Give the extent of all Plasmodium ovale-infected red blood cells.
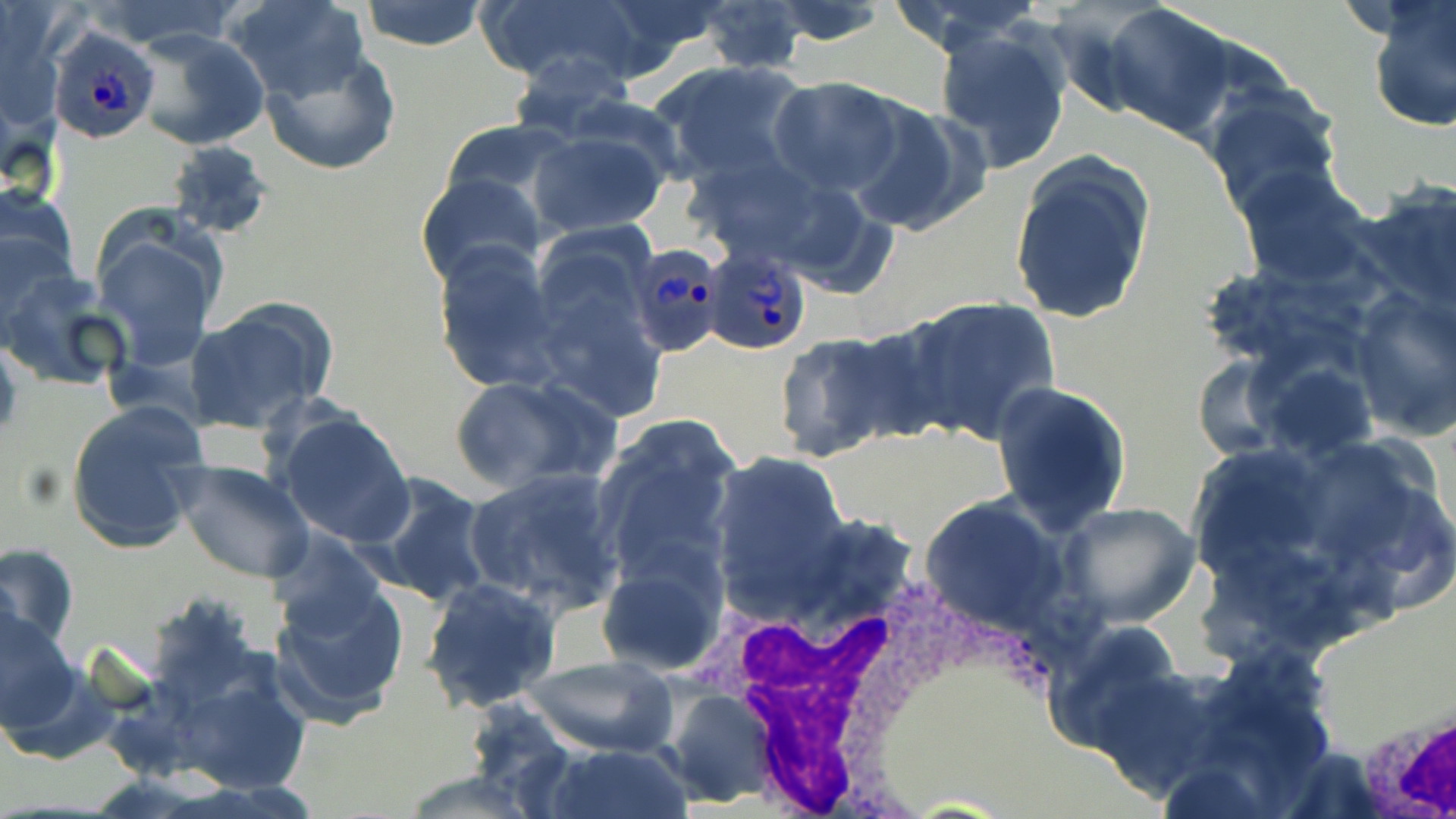
Approximate bounding boxes as [x1, y1, x2, y2] in pixels.
Plasmodium ovale-infected red blood cells: [47, 25, 163, 145], [633, 240, 723, 363], [701, 246, 815, 357].

slide-level diagnosis = Plasmodium ovale
stain = May-Grünwald-Giemsa
modality = optical microscopy
magnification = 1000x
uninfected red blood cell locations = approximate bounding boxes as [x1, y1, x2, y2] in pixels: [228, 0, 373, 105], [358, 0, 489, 52], [475, 0, 653, 91], [883, 0, 1050, 53], [1365, 0, 1455, 132], [693, 1, 811, 75], [764, 2, 893, 47], [1102, 3, 1236, 141], [933, 25, 1072, 174], [131, 29, 270, 152], [261, 51, 400, 177], [505, 52, 637, 140], [651, 59, 813, 188], [768, 76, 909, 198], [1199, 85, 1345, 216], [847, 99, 987, 238], [438, 119, 583, 217], [528, 125, 673, 237], [165, 139, 273, 241], [1009, 155, 1155, 324], [1234, 165, 1373, 289], [416, 174, 548, 292], [1356, 179, 1456, 309], [0, 185, 83, 319], [92, 220, 225, 372], [431, 241, 563, 393], [2, 273, 133, 393], [1347, 288, 1456, 441], [897, 297, 1061, 445], [181, 299, 336, 436], [769, 332, 913, 464], [0, 337, 21, 447], [1188, 350, 1296, 460], [1252, 359, 1381, 464], [447, 373, 614, 494], [991, 379, 1132, 536], [65, 401, 209, 556], [271, 408, 415, 548], [590, 415, 743, 588], [1187, 432, 1456, 635], [1184, 443, 1337, 589], [706, 453, 850, 608], [171, 460, 314, 584], [463, 467, 627, 616], [357, 473, 496, 607], [919, 497, 1077, 640], [1057, 502, 1203, 629], [0, 541, 80, 655], [595, 551, 730, 676], [267, 567, 411, 724], [419, 577, 561, 712], [0, 605, 83, 738], [1045, 620, 1187, 753], [152, 650, 316, 801], [525, 653, 678, 757], [659, 687, 778, 807], [541, 743, 691, 819], [396, 770, 550, 818]
image size = 1456×819 pixels
field of view = one of a larger specimen
white blood cell locations = approximate bounding boxes as [x1, y1, x2, y2] in pixels: [714, 557, 994, 816], [1355, 697, 1456, 814]
preparation = thin blood smear